Identify the parasite.
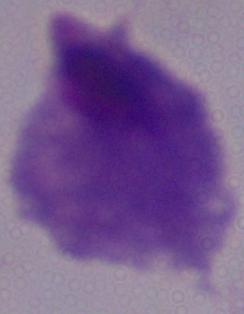

A trichomonad.

Photomicrograph. 1000x magnification.